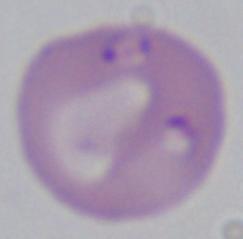

identification = Babesia
modality = micrograph
magnification = 1000x